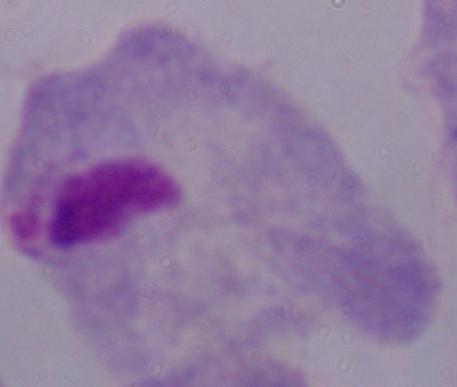
identification: trichomonad
modality: micrograph
magnification: 1000x